Comment on the morphology of the red blood cells.
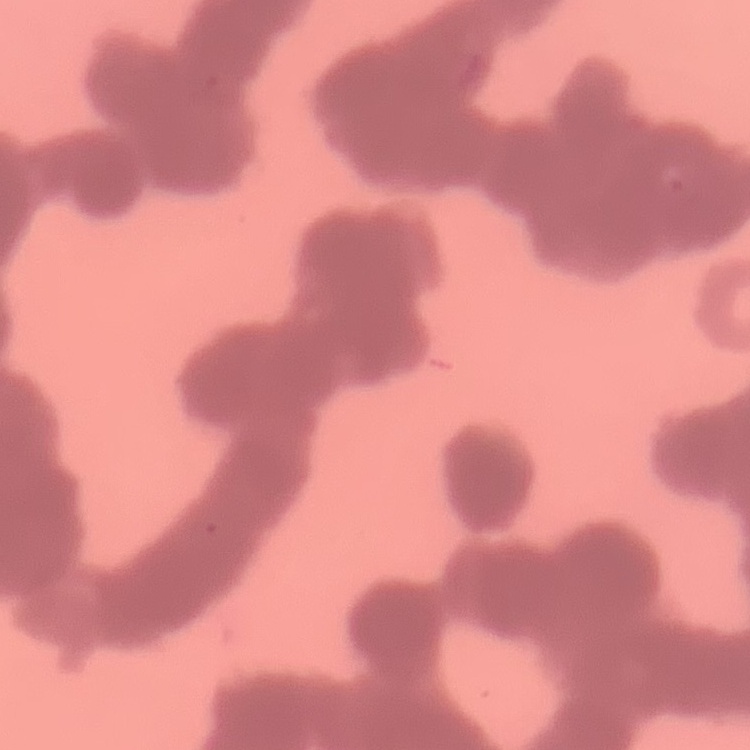

They show rouleaux formation.

Field's or Giemsa stain. One tile cut from a larger photomicrograph. Thin blood smear.